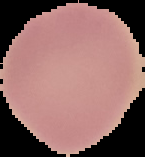
Summary:
  - Image size: 145×157 pixels
  - Preparation: thin blood film
  - Malaria status: uninfected
  - Image type: segmented cell region on a black background